Give the extent of all Plasmodium ovale-infected red blood cells.
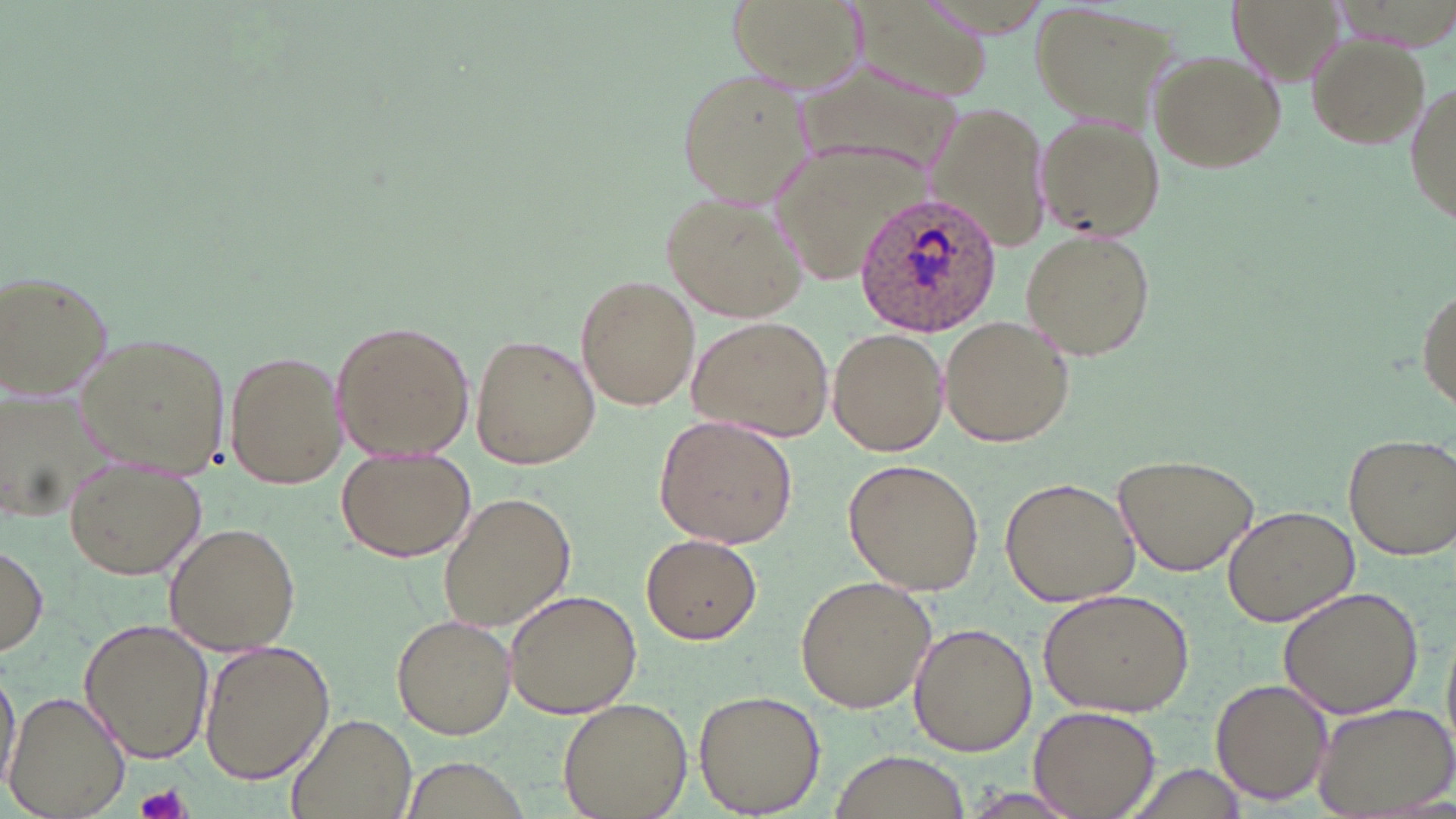
Approximate bounding boxes as (x1, y1, x2, y2) in pixels.
Plasmodium ovale-infected red blood cells: (854, 191, 1008, 338).

Summary:
  - Platelet locations: (138, 783, 189, 819)
  - Uninfected red blood cell locations: (723, 0, 867, 97), (849, 0, 995, 105), (1229, 0, 1342, 86), (1030, 4, 1180, 124), (1306, 34, 1429, 149), (1147, 48, 1286, 173), (797, 55, 962, 181), (675, 65, 816, 206), (1404, 77, 1456, 233), (924, 103, 1053, 253), (1035, 115, 1167, 243), (769, 141, 907, 283), (663, 188, 809, 323), (1020, 228, 1157, 359), (0, 270, 117, 402), (575, 274, 699, 410), (1415, 279, 1455, 414), (939, 315, 1075, 447), (688, 316, 834, 441), (330, 320, 476, 461), (826, 326, 950, 457), (73, 329, 232, 478), (470, 332, 599, 470), (223, 347, 346, 488), (2, 389, 123, 525), (652, 414, 800, 549), (1342, 430, 1456, 559), (14, 439, 169, 565), (336, 448, 477, 563), (1115, 452, 1261, 575), (63, 454, 209, 579), (845, 457, 987, 596), (1001, 475, 1139, 608), (436, 490, 577, 631), (1222, 505, 1359, 626), (161, 522, 302, 655), (640, 533, 762, 644), (1, 540, 49, 658), (796, 574, 934, 715), (1279, 584, 1425, 719), (504, 588, 642, 720), (1039, 588, 1192, 718), (391, 614, 516, 739), (78, 618, 213, 765), (910, 623, 1036, 756), (197, 641, 334, 783), (0, 662, 20, 794), (1211, 678, 1331, 806), (693, 689, 824, 815), (4, 690, 129, 819), (557, 697, 693, 819), (1309, 701, 1455, 817), (1030, 705, 1159, 818), (287, 712, 418, 819), (831, 751, 968, 818)
  - Slide-level diagnosis: Plasmodium ovale
  - Preparation: thin blood smear
  - Field of view: single
  - Stain: May-Grünwald-Giemsa
  - Magnification: 1000x
  - Image size: 1456×819 pixels
  - Modality: optical microscopy